Locate every blood parasite and identify its species.
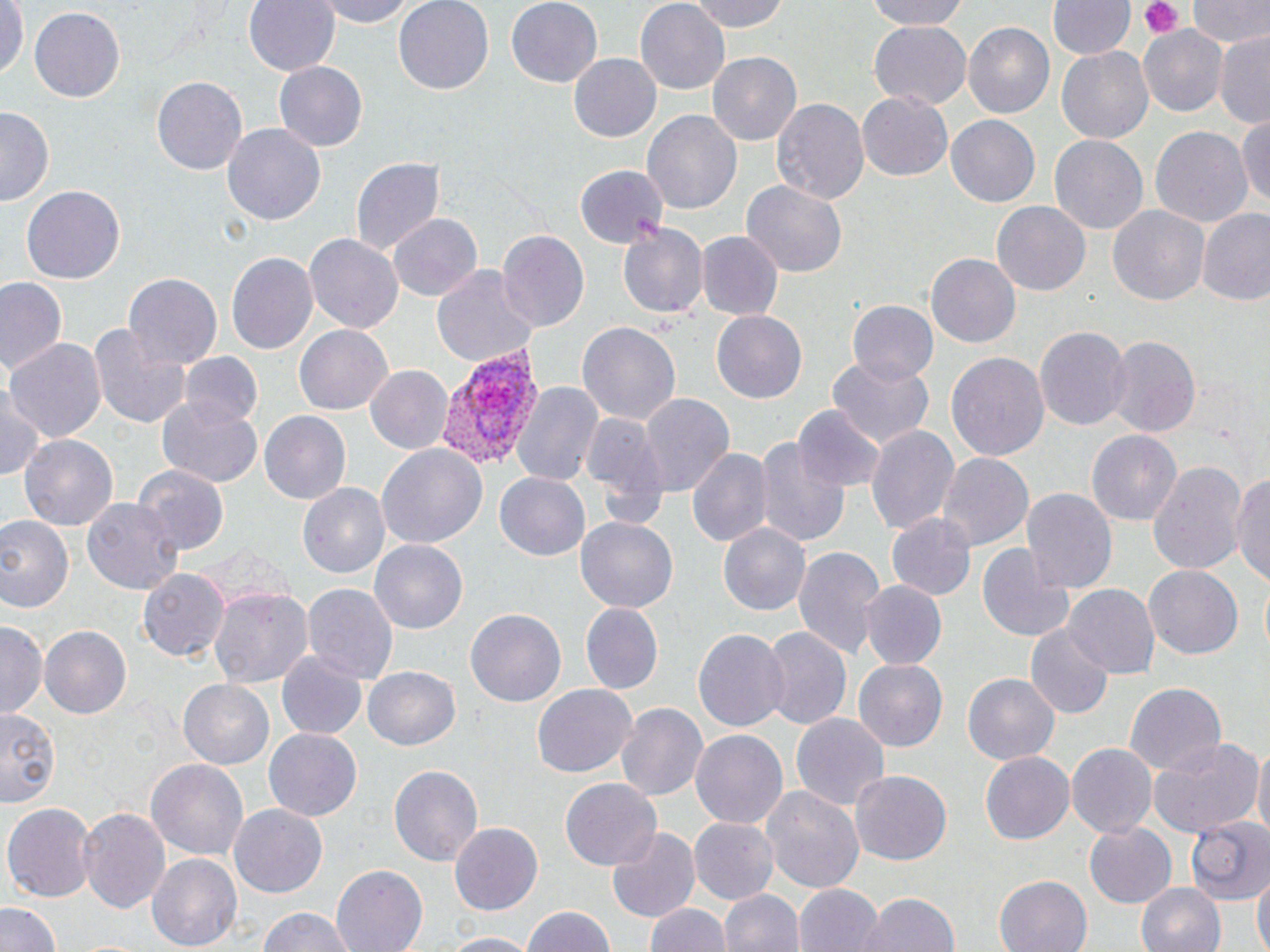

Approximate bounding boxes as named x1/y1/x2/y2 corners in pixels.
Plasmodium vivax-infected red blood cells: (x1=435, y1=343, x2=545, y2=470).
No Plasmodium falciparum, Plasmodium ovale, Plasmodium malariae, Babesia divergens, or Trypanosoma brucei observed.

Summary:
  - Platelet locations: (x1=1140, y1=0, x2=1186, y2=38)
  - Uninfected red blood cell locations: (x1=245, y1=0, x2=340, y2=77), (x1=313, y1=0, x2=415, y2=26), (x1=393, y1=0, x2=496, y2=92), (x1=506, y1=0, x2=602, y2=88), (x1=687, y1=0, x2=789, y2=33), (x1=856, y1=0, x2=977, y2=30), (x1=1188, y1=0, x2=1269, y2=50), (x1=1050, y1=1, x2=1133, y2=62), (x1=0, y1=2, x2=25, y2=82), (x1=634, y1=2, x2=728, y2=88), (x1=30, y1=8, x2=123, y2=103), (x1=867, y1=21, x2=971, y2=111), (x1=961, y1=22, x2=1055, y2=121), (x1=1137, y1=26, x2=1228, y2=117), (x1=1214, y1=30, x2=1270, y2=125), (x1=1055, y1=44, x2=1154, y2=145), (x1=708, y1=51, x2=801, y2=145), (x1=569, y1=53, x2=661, y2=142), (x1=274, y1=61, x2=369, y2=152), (x1=152, y1=76, x2=245, y2=176), (x1=857, y1=90, x2=954, y2=180), (x1=771, y1=96, x2=868, y2=206), (x1=0, y1=107, x2=53, y2=209), (x1=642, y1=108, x2=742, y2=215), (x1=1237, y1=113, x2=1270, y2=215), (x1=946, y1=115, x2=1040, y2=207), (x1=224, y1=123, x2=326, y2=225), (x1=1148, y1=124, x2=1253, y2=226), (x1=1051, y1=135, x2=1148, y2=236), (x1=351, y1=157, x2=444, y2=258), (x1=576, y1=167, x2=667, y2=247), (x1=741, y1=178, x2=850, y2=279), (x1=21, y1=186, x2=123, y2=286), (x1=992, y1=201, x2=1090, y2=295), (x1=1108, y1=206, x2=1209, y2=307), (x1=1196, y1=208, x2=1270, y2=305), (x1=389, y1=213, x2=482, y2=301), (x1=616, y1=223, x2=707, y2=319), (x1=498, y1=232, x2=589, y2=333), (x1=696, y1=232, x2=782, y2=320), (x1=306, y1=234, x2=402, y2=334), (x1=226, y1=251, x2=318, y2=355), (x1=927, y1=254, x2=1020, y2=348), (x1=430, y1=261, x2=539, y2=371), (x1=124, y1=272, x2=222, y2=368), (x1=0, y1=277, x2=68, y2=373), (x1=847, y1=301, x2=938, y2=386), (x1=711, y1=311, x2=809, y2=403), (x1=92, y1=320, x2=190, y2=430), (x1=575, y1=320, x2=681, y2=427), (x1=294, y1=325, x2=393, y2=416), (x1=1034, y1=325, x2=1130, y2=431), (x1=1105, y1=335, x2=1200, y2=437), (x1=6, y1=337, x2=106, y2=441), (x1=947, y1=351, x2=1050, y2=465), (x1=180, y1=353, x2=263, y2=431), (x1=827, y1=357, x2=935, y2=447), (x1=364, y1=365, x2=451, y2=455), (x1=514, y1=380, x2=602, y2=488), (x1=0, y1=388, x2=47, y2=483), (x1=640, y1=393, x2=734, y2=496), (x1=156, y1=398, x2=264, y2=488), (x1=793, y1=405, x2=885, y2=497), (x1=580, y1=411, x2=670, y2=504), (x1=260, y1=413, x2=350, y2=503), (x1=865, y1=422, x2=959, y2=534), (x1=1088, y1=429, x2=1181, y2=525), (x1=18, y1=431, x2=119, y2=530), (x1=756, y1=436, x2=847, y2=548), (x1=377, y1=443, x2=487, y2=550), (x1=687, y1=445, x2=773, y2=550), (x1=938, y1=451, x2=1034, y2=552), (x1=1148, y1=458, x2=1247, y2=579), (x1=135, y1=465, x2=229, y2=552), (x1=1232, y1=468, x2=1270, y2=592), (x1=494, y1=472, x2=591, y2=563), (x1=297, y1=482, x2=389, y2=579), (x1=1022, y1=487, x2=1117, y2=593), (x1=81, y1=495, x2=185, y2=593), (x1=0, y1=513, x2=75, y2=615), (x1=887, y1=514, x2=975, y2=600), (x1=577, y1=516, x2=678, y2=613), (x1=719, y1=521, x2=811, y2=615), (x1=370, y1=536, x2=468, y2=631), (x1=977, y1=539, x2=1076, y2=643), (x1=792, y1=543, x2=883, y2=659), (x1=1145, y1=565, x2=1242, y2=660), (x1=138, y1=567, x2=227, y2=661), (x1=862, y1=581, x2=945, y2=669), (x1=304, y1=582, x2=397, y2=685), (x1=1063, y1=583, x2=1159, y2=679), (x1=207, y1=585, x2=313, y2=687), (x1=577, y1=602, x2=663, y2=693), (x1=466, y1=606, x2=566, y2=707), (x1=0, y1=620, x2=47, y2=717), (x1=1027, y1=625, x2=1113, y2=720), (x1=42, y1=626, x2=131, y2=718), (x1=759, y1=626, x2=850, y2=733), (x1=692, y1=628, x2=789, y2=734), (x1=277, y1=650, x2=368, y2=741), (x1=854, y1=660, x2=947, y2=750), (x1=363, y1=666, x2=464, y2=752), (x1=963, y1=673, x2=1059, y2=764), (x1=178, y1=679, x2=274, y2=769), (x1=1121, y1=682, x2=1225, y2=777), (x1=533, y1=684, x2=636, y2=778), (x1=615, y1=701, x2=708, y2=802), (x1=0, y1=711, x2=61, y2=806), (x1=792, y1=712, x2=889, y2=813), (x1=690, y1=727, x2=787, y2=827), (x1=263, y1=728, x2=362, y2=822), (x1=1150, y1=737, x2=1263, y2=837), (x1=1250, y1=739, x2=1270, y2=844), (x1=1067, y1=743, x2=1158, y2=838), (x1=980, y1=753, x2=1073, y2=844), (x1=145, y1=754, x2=248, y2=860), (x1=388, y1=762, x2=483, y2=866), (x1=849, y1=769, x2=950, y2=865), (x1=560, y1=778, x2=661, y2=870), (x1=762, y1=788, x2=863, y2=891), (x1=3, y1=801, x2=94, y2=900), (x1=76, y1=804, x2=170, y2=913), (x1=230, y1=804, x2=328, y2=898), (x1=1186, y1=813, x2=1270, y2=903), (x1=690, y1=818, x2=774, y2=903), (x1=1083, y1=822, x2=1177, y2=909), (x1=450, y1=823, x2=544, y2=916), (x1=607, y1=826, x2=700, y2=923), (x1=148, y1=852, x2=242, y2=951), (x1=330, y1=865, x2=427, y2=952), (x1=994, y1=873, x2=1090, y2=952), (x1=1253, y1=873, x2=1269, y2=952), (x1=1136, y1=881, x2=1227, y2=952), (x1=794, y1=884, x2=882, y2=952), (x1=720, y1=889, x2=801, y2=952), (x1=859, y1=890, x2=960, y2=952), (x1=644, y1=900, x2=729, y2=952), (x1=0, y1=901, x2=60, y2=952), (x1=519, y1=905, x2=616, y2=952), (x1=253, y1=909, x2=358, y2=952), (x1=438, y1=933, x2=539, y2=952)
  - Slide-level diagnosis: Plasmodium vivax
  - Image size: 1270×952 pixels
  - Modality: light microscopy
  - Field of view: single
  - Preparation: thin blood film
  - Magnification: 1000x
  - Stain: May-Grünwald-Giemsa